Report the malaria status of this cell.
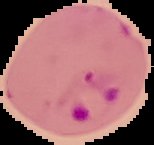

It is parasitized.

image type = segmented cell region on a black background
image size = 154×145 pixels
preparation = thin blood film